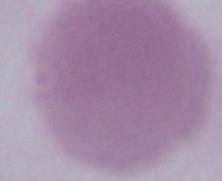

A red blood cell is shown. Captured at 1000x magnification. Micrograph.